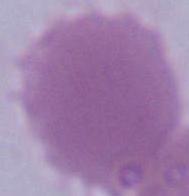
Photomicrograph. A red blood cell is shown. 1000x magnification.